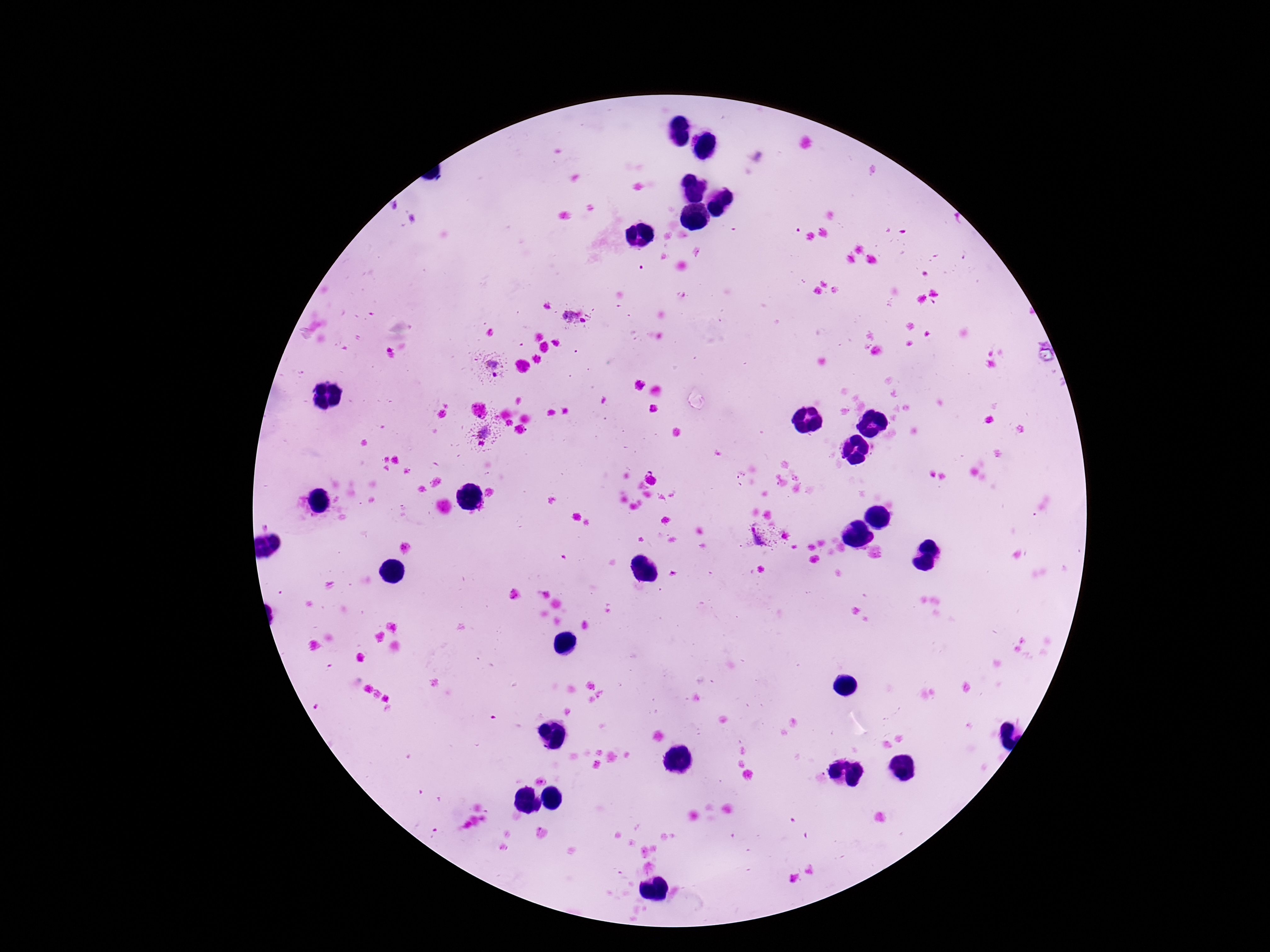

Approximate centers as [x, y] in pixels.
Summary:
  - Plasmodium parasite locations: [576, 318], [491, 369], [483, 435], [762, 537]
  - Preparation: thick blood film
  - Image size: 1270×952 pixels
  - Stain: Giemsa
  - Capture: smartphone camera through the microscope eyepiece
  - Patient malaria status: positive
  - Field of view: one from this slide
  - Magnification: 100x